Report the malaria status of this cell.
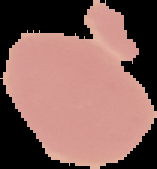
It is uninfected.

image type = cell region segmented out of the field of view; surrounding area masked to black
preparation = thin blood film
image size = 157×169 pixels